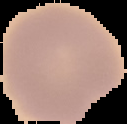

Summary:
  - Image size: 127×124 pixels
  - Preparation: thin blood film
  - Result: no malaria parasites seen
  - Image type: segmented cell region with the area outside set to black